Point out each leukocyte.
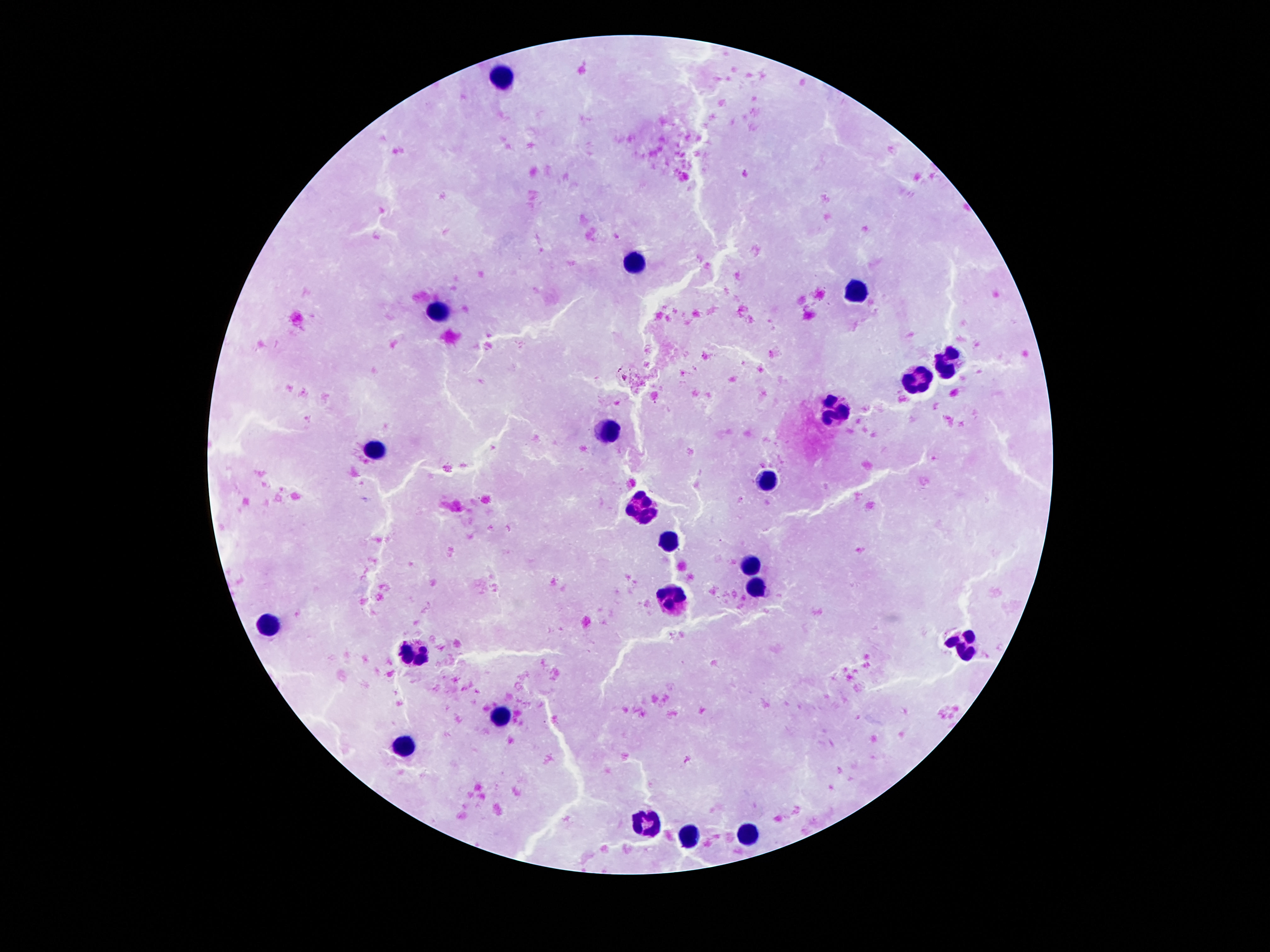
Approximate centers as (x, y) in pixels.
Leukocytes: (502, 75), (633, 263), (855, 292), (441, 309), (949, 362), (918, 378), (836, 413), (611, 430), (375, 449), (767, 477), (642, 503), (666, 542), (754, 563), (758, 589), (670, 598), (271, 622), (961, 645), (412, 650), (502, 714), (406, 747), (646, 825), (744, 828), (689, 837).

Patient malaria status: uninfected. Image is 1270×952 pixels. Single field of view. 100x magnification. Thick blood smear. Smartphone photograph taken through the microscope eyepiece. Giemsa stain.